Report the malaria status of this cell.
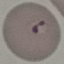
Parasitized.

Automatically extracted cell patch, resized to 64 × 64 pixels. Thin blood smear. Giemsa-stained preparation. Photographed with a smartphone camera at the microscope eyepiece.